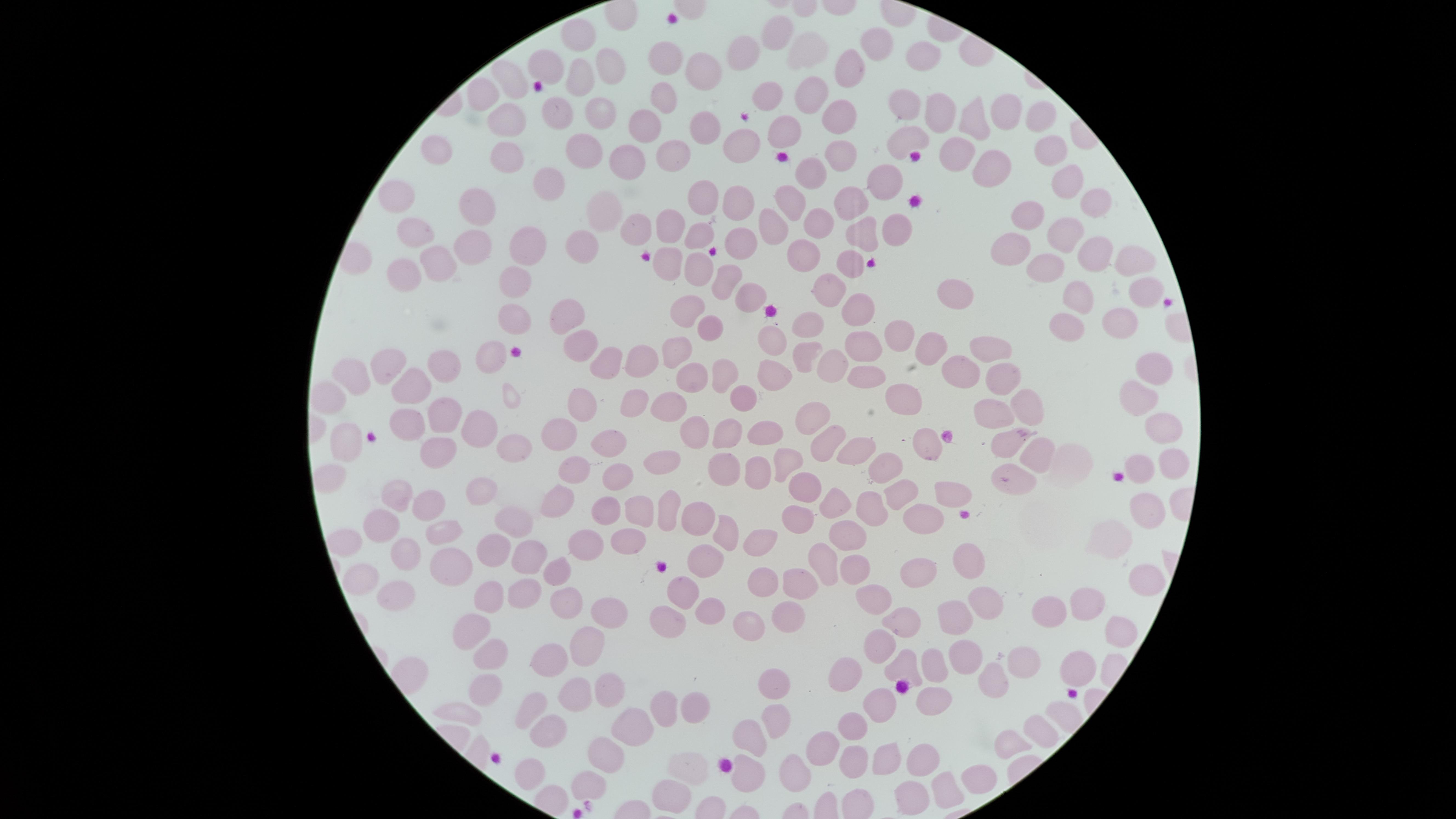

Approximate marker points as (x, y) in pixels. Uninfected red blood cells: (579, 33), (778, 33), (881, 39), (750, 52), (811, 52), (670, 58), (927, 59), (541, 66), (607, 69), (850, 71), (701, 73), (507, 78), (579, 78), (481, 90), (812, 91), (770, 92), (661, 98), (601, 107), (558, 110), (909, 111), (830, 113), (941, 113), (1005, 115), (508, 117), (974, 119), (1040, 120), (644, 125), (704, 129), (909, 136), (741, 139), (780, 140), (438, 147), (505, 149), (580, 149), (1053, 151), (835, 152), (953, 153), (673, 154), (632, 157), (983, 166), (810, 173), (544, 176), (890, 176), (1064, 185), (402, 194), (845, 194), (701, 197), (735, 199), (787, 202), (479, 205), (1096, 205), (601, 206), (1030, 215), (821, 218), (894, 220), (637, 223), (772, 226), (662, 228), (866, 230), (414, 231), (1064, 231), (698, 233), (524, 237), (738, 237), (472, 239), (575, 241), (1012, 248), (801, 251), (1094, 252), (843, 257), (670, 259), (1126, 260), (437, 263), (696, 268), (1046, 271), (399, 273), (723, 278), (515, 283), (827, 289), (1145, 289), (953, 290), (1075, 294), (749, 295), (692, 305), (857, 306), (566, 313), (1120, 317), (518, 318), (808, 323), (1068, 325), (709, 329), (901, 329), (772, 335), (580, 340), (931, 345), (993, 345), (867, 347), (679, 348), (492, 350), (390, 351), (799, 354), (607, 359), (641, 360), (832, 363), (444, 365), (1153, 365), (352, 367), (961, 368), (775, 370), (870, 373), (1003, 374), (718, 375), (692, 378), (410, 384), (630, 393), (744, 393), (575, 394), (1135, 394), (1025, 398), (907, 402), (671, 406), (443, 415), (816, 415), (988, 417), (406, 421), (480, 427), (693, 427), (1158, 428), (726, 431), (559, 434), (760, 437), (828, 441), (510, 442), (1004, 442), (606, 443), (926, 443), (344, 444), (857, 446), (434, 447), (660, 454), (791, 454), (1034, 460), (1145, 460), (890, 463), (1171, 465), (577, 467), (722, 467), (752, 473), (329, 477), (610, 479), (1013, 482), (475, 489), (802, 489), (897, 491), (946, 491), (400, 494), (429, 500), (838, 500), (555, 501), (1145, 506), (641, 507), (671, 507), (602, 508), (866, 509), (798, 514), (926, 518), (698, 519), (512, 523), (381, 525), (441, 526), (724, 529), (628, 535), (850, 536), (579, 540), (756, 540), (490, 545), (402, 552), (708, 558), (525, 559), (815, 559), (964, 560), (445, 562), (846, 564), (556, 570), (915, 574), (355, 576), (1142, 579), (759, 582), (797, 583), (389, 593), (684, 593), (520, 599), (557, 600), (876, 601), (985, 601), (1083, 601), (485, 605), (598, 608), (705, 611), (1057, 612), (786, 618), (907, 619), (949, 619), (742, 622), (669, 630), (468, 631), (1115, 635), (879, 639), (584, 646), (965, 649), (487, 650), (1024, 658), (545, 660), (904, 663), (932, 666), (1075, 668), (851, 670), (988, 679), (769, 685), (486, 688), (613, 691), (567, 695), (930, 702), (528, 703), (662, 705), (695, 709), (463, 710), (878, 710), (771, 719), (1040, 721), (636, 726), (847, 727), (547, 730), (750, 732), (1012, 739), (608, 750), (818, 750), (928, 757), (850, 762), (889, 762), (528, 772), (689, 773), (781, 773), (741, 776), (974, 778), (588, 780), (949, 788), (669, 794), (911, 797). Giemsa-stained preparation. Thin blood smear. One field of view of the specimen. The visible region is circular. Image is 1456×819 pixels. Smartphone photograph through the microscope eyepiece. Presence: no malaria parasites identified.